Assess this cell for malaria.
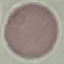

Uninfected.

Giemsa-stained preparation. Photographed with a smartphone camera at the microscope eyepiece. Thin smear of blood. Cell patch, automatically extracted from a larger field of view and resized to 64 × 64 pixels.